Classify this cell by malaria status.
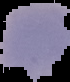

Parasitized.

Summary:
  - Preparation: thin blood film
  - Image size: 70×82 pixels
  - Image type: cell region segmented out of the field of view; surrounding area masked to black